Point out each leukocyte.
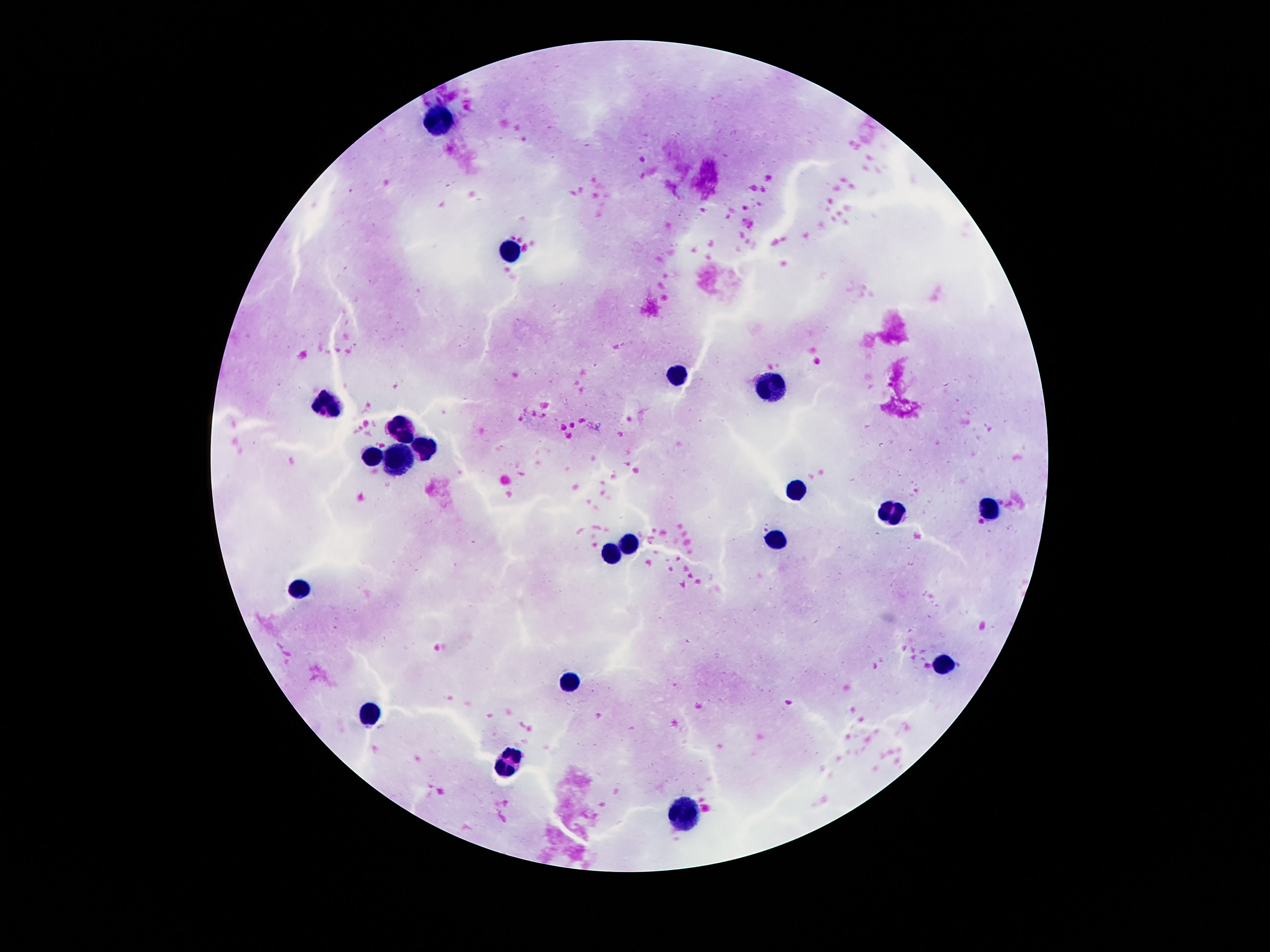
Approximate centers as {x, y} in pixels.
Leukocytes: {439, 122}, {510, 249}, {676, 374}, {770, 385}, {325, 404}, {401, 433}, {426, 447}, {372, 459}, {399, 459}, {800, 491}, {989, 510}, {888, 513}, {632, 540}, {775, 540}, {613, 552}, {300, 591}, {942, 664}, {571, 681}, {369, 712}, {506, 762}, {686, 811}.

Summary:
  - Preparation: thick blood smear
  - Patient malaria status: uninfected
  - Magnification: 100x
  - Stain: Giemsa
  - Capture: smartphone camera through the microscope eyepiece
  - Field of view: one from this slide
  - Image size: 1270×952 pixels